Classify this cell by malaria status.
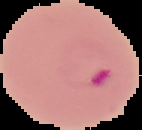

It is parasitized.

image type = segmented cell region with the area outside set to black
image size = 142×130 pixels
preparation = thin blood film